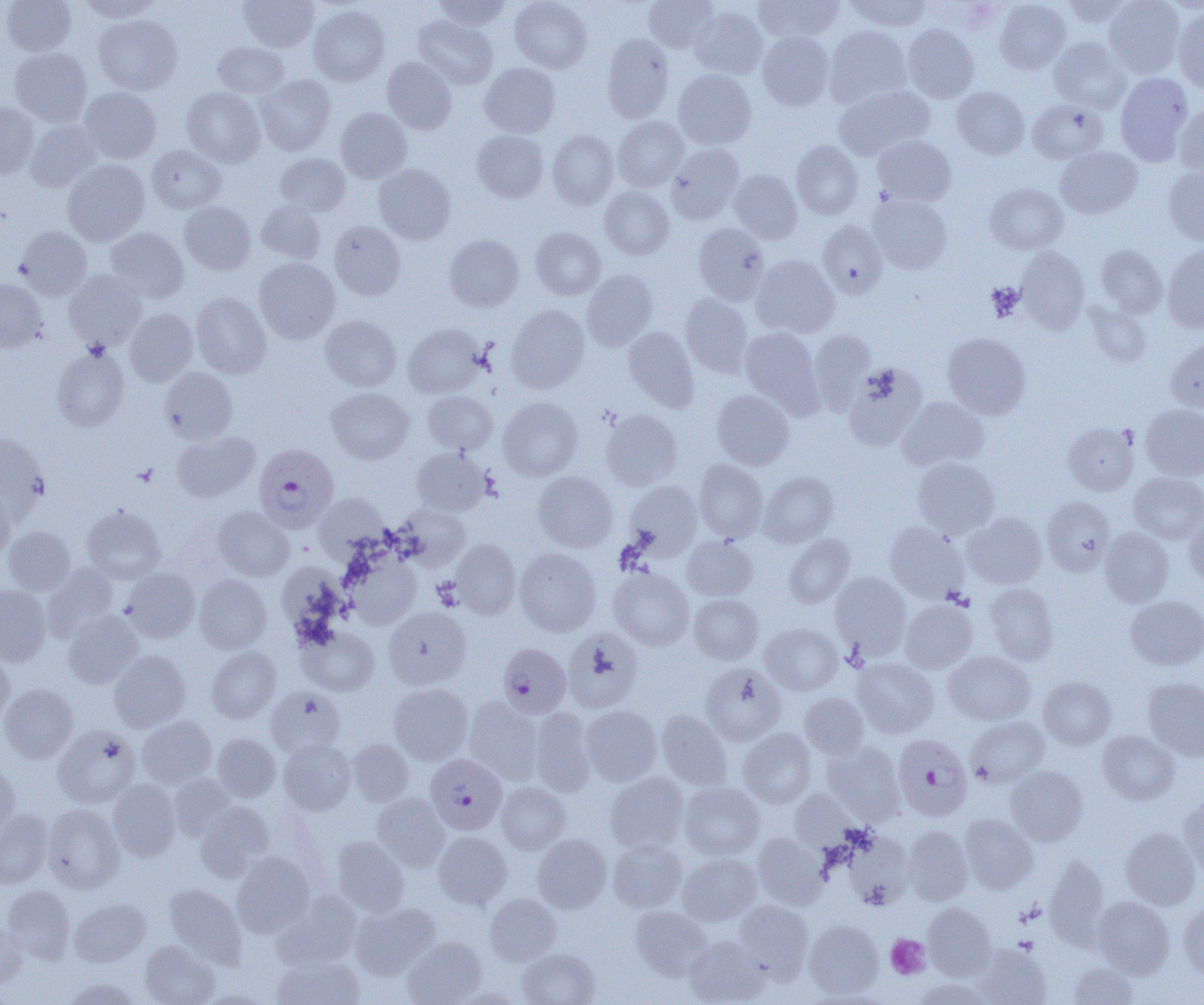

Summary:
  - Coordinate format: approximate bounding boxes as (x1,y1)-(x2,y2) corner pairs in pixels
  - Platelet locations: (986,282)-(1024,320), (886,935)-(930,979)
  - Uninfected red blood cell locations: (2,0)-(76,56), (78,0)-(164,22), (238,0)-(319,52), (433,0)-(510,31), (510,0)-(592,73), (643,0)-(718,52), (753,0)-(844,42), (844,0)-(932,32), (994,0)-(1071,73), (1060,0)-(1135,28), (1104,0)-(1186,78), (308,5)-(389,86), (690,6)-(768,79), (1173,6)-(1204,94), (94,14)-(182,95), (413,15)-(498,90), (903,24)-(979,103), (824,26)-(912,107), (757,31)-(833,110), (602,34)-(673,123), (1049,37)-(1130,112), (213,42)-(289,98), (10,47)-(92,126), (382,57)-(457,134), (479,62)-(560,138), (674,70)-(756,149), (1115,73)-(1193,165), (256,74)-(336,156), (834,85)-(934,160), (952,86)-(1029,159), (80,87)-(161,163), (182,87)-(265,167), (1028,99)-(1108,164), (0,103)-(39,178), (1174,104)-(1204,178), (336,108)-(412,183), (612,117)-(688,191), (25,120)-(102,192), (472,130)-(548,202), (547,130)-(618,209), (873,135)-(957,206), (791,140)-(864,219), (666,143)-(744,223), (147,145)-(225,213), (1056,146)-(1142,218), (275,153)-(350,216), (62,159)-(150,246), (374,164)-(455,244), (1163,164)-(1204,245), (729,169)-(802,243), (985,184)-(1067,254), (600,186)-(674,260), (868,194)-(952,274), (179,201)-(255,274), (257,201)-(326,264), (329,221)-(405,300), (818,221)-(888,298), (693,223)-(769,305), (16,226)-(92,299), (106,227)-(189,303), (531,228)-(605,300), (444,234)-(524,311), (1096,245)-(1168,317), (1162,245)-(1204,333), (1015,247)-(1089,333), (751,255)-(839,338), (254,258)-(340,343), (581,270)-(658,351), (64,271)-(147,350), (0,279)-(47,352), (191,292)-(271,378), (680,293)-(753,377), (1086,303)-(1151,367), (506,305)-(589,393), (125,309)-(198,385), (320,315)-(401,391), (403,323)-(484,398), (624,327)-(699,412), (739,328)-(822,414), (808,330)-(876,414), (942,332)-(1031,419), (1166,338)-(1204,412), (52,346)-(129,431), (843,364)-(926,451), (160,368)-(237,442), (326,387)-(414,463), (712,390)-(794,470), (423,391)-(498,454), (898,396)-(989,471), (498,397)-(582,481), (1141,404)-(1204,480), (600,408)-(682,490), (1063,422)-(1139,495), (172,431)-(260,502), (0,434)-(49,521), (411,448)-(490,516), (912,456)-(1000,538), (694,459)-(768,543), (759,471)-(839,547), (533,472)-(617,552), (1129,472)-(1204,544), (624,481)-(702,560), (0,485)-(14,563), (313,492)-(389,561), (1042,496)-(1115,575), (81,505)-(165,583), (396,505)-(470,568), (214,506)-(295,580), (963,512)-(1047,589), (1183,513)-(1204,587), (885,521)-(968,603), (2,526)-(76,596), (1100,527)-(1174,607), (784,534)-(855,608), (682,536)-(757,601), (453,539)-(521,619), (514,548)-(601,636), (344,551)-(421,629), (42,563)-(118,639), (608,567)-(694,650), (122,568)-(200,642), (830,571)-(910,657), (195,574)-(272,653), (983,583)-(1058,665), (0,585)-(51,666), (688,594)-(763,664), (1125,595)-(1204,670), (899,599)-(977,673), (383,607)-(471,688), (63,610)-(143,688), (760,622)-(842,696), (298,626)-(378,696), (562,629)-(642,712), (207,646)-(280,723), (109,650)-(190,732), (0,651)-(14,721), (944,651)-(1035,725), (852,657)-(938,738), (700,663)-(786,745), (1039,676)-(1116,749), (1143,677)-(1204,761), (0,683)-(78,762), (388,683)-(473,764), (266,687)-(345,757), (800,693)-(869,759), (464,696)-(543,783), (581,705)-(661,785), (529,708)-(596,795), (657,710)-(732,790), (138,715)-(216,787), (966,716)-(1048,788), (53,725)-(140,807), (738,728)-(816,808), (1098,729)-(1180,804), (213,733)-(281,801), (279,739)-(355,814), (347,740)-(413,805), (822,741)-(905,823), (0,760)-(20,838), (1006,766)-(1088,845), (169,773)-(235,839), (605,773)-(689,853), (108,779)-(181,861), (496,782)-(570,853), (679,783)-(764,860), (789,788)-(858,852), (372,793)-(450,871), (1178,794)-(1204,878), (195,801)-(274,881), (43,804)-(124,893), (0,810)-(53,888), (960,814)-(1038,893), (903,826)-(973,905), (1120,827)-(1201,910), (433,831)-(512,909), (753,832)-(829,909), (844,832)-(914,908), (532,834)-(611,912), (332,835)-(409,914), (608,838)-(686,912), (679,852)-(761,925), (232,853)-(314,936), (1044,856)-(1110,948), (164,883)-(246,966), (2,885)-(75,964), (273,890)-(361,968), (485,893)-(561,965), (1092,896)-(1174,978), (70,898)-(151,966), (734,900)-(813,979), (1179,900)-(1204,980), (351,902)-(440,979), (923,903)-(995,979), (631,906)-(712,980), (804,920)-(883,998), (0,923)-(26,989), (684,935)-(769,1004), (403,936)-(486,1005), (139,940)-(219,1005), (974,943)-(1051,1005), (518,948)-(599,1005), (272,955)-(364,1005), (1067,961)-(1139,1004), (62,977)-(144,1004), (914,977)-(991,1005), (453,988)-(525,1005)
  - Plasmodium falciparum-infected red blood cell locations: (259,442)-(339,533), (498,643)-(571,718), (893,734)-(973,821), (426,748)-(507,832)
  - Slide-level diagnosis: Plasmodium falciparum
  - Preparation: thin blood film
  - Field of view: single
  - Magnification: 1000x
  - Image size: 1204×1005 pixels
  - Modality: light microscopy